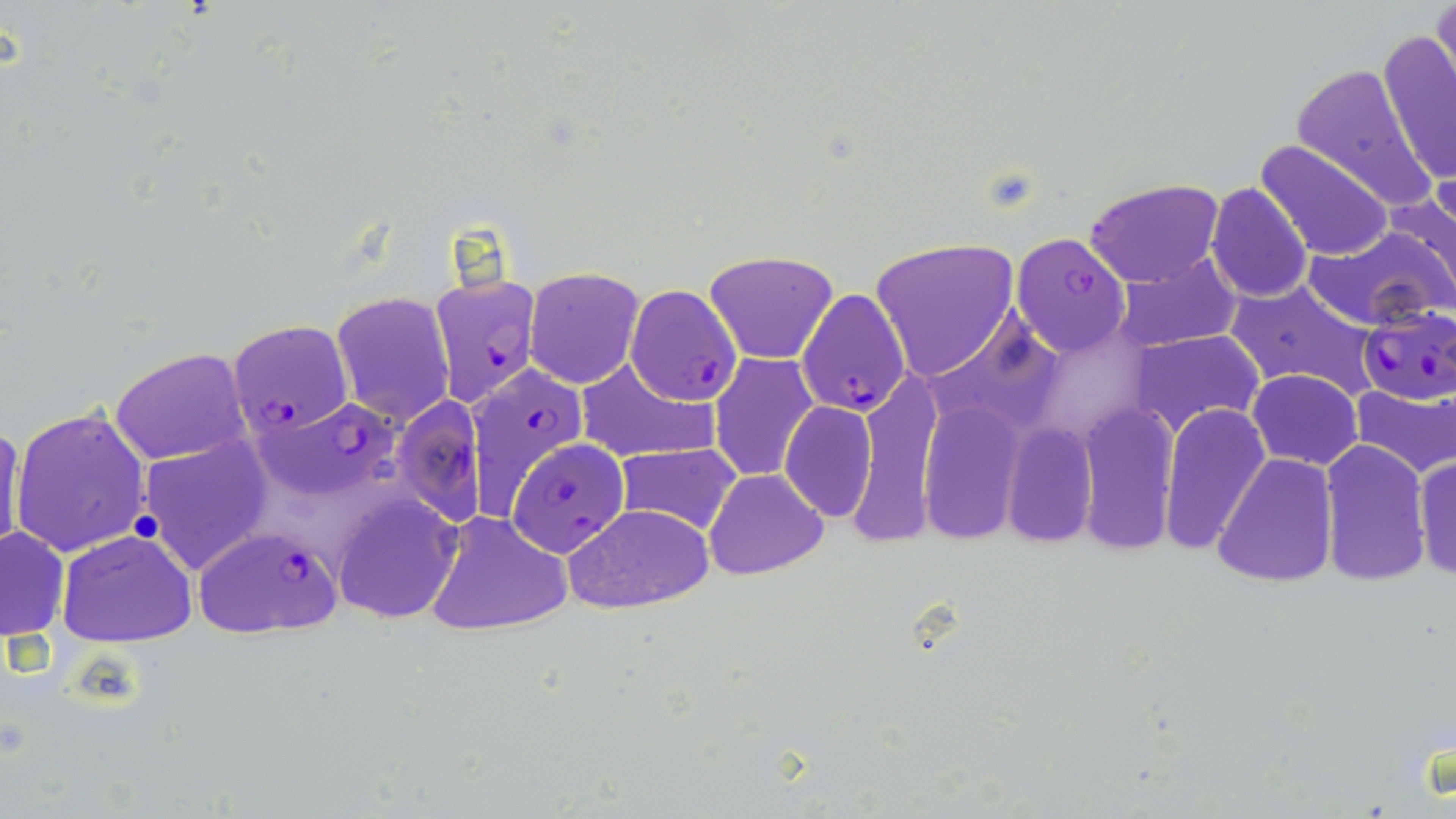
Plasmodium falciparum-infected red blood cell locations = approximate bounding boxes as (x1, y1, x2, y2) in pixels: (1010, 231, 1131, 357), (428, 274, 541, 407), (626, 284, 741, 405), (798, 288, 911, 417), (1357, 306, 1456, 404), (228, 319, 353, 436), (465, 366, 589, 510), (394, 395, 486, 526), (261, 399, 395, 489), (508, 438, 629, 556), (194, 526, 343, 638)
slide-level diagnosis = Plasmodium falciparum
stain = May-Grünwald-Giemsa
preparation = thin blood smear
field of view = single
uninfected red blood cell locations = approximate bounding boxes as (x1, y1, x2, y2) in pixels: (1431, 0, 1456, 97), (1378, 28, 1456, 188), (1255, 139, 1392, 260), (1083, 177, 1225, 286), (1205, 182, 1314, 304), (1388, 184, 1456, 308), (1303, 226, 1451, 331), (869, 236, 1018, 382), (704, 247, 840, 364), (1115, 255, 1242, 352), (525, 266, 644, 389), (1225, 279, 1381, 402), (330, 292, 455, 427), (1132, 330, 1264, 434), (110, 347, 250, 466), (707, 353, 819, 482), (573, 358, 718, 462), (1247, 369, 1362, 469), (1350, 380, 1456, 477), (777, 400, 877, 521), (916, 402, 1025, 543), (1081, 402, 1181, 550), (1159, 402, 1270, 552), (9, 405, 152, 558), (0, 419, 25, 560), (1001, 423, 1097, 550), (133, 438, 272, 575), (1319, 438, 1431, 586), (614, 444, 742, 535), (1413, 451, 1455, 583), (1211, 454, 1336, 588), (705, 468, 829, 580), (332, 494, 463, 624), (564, 502, 715, 614), (425, 511, 571, 636), (0, 525, 70, 641), (57, 529, 200, 646)
magnification = 1000x
modality = optical microscopy
image size = 1456×819 pixels